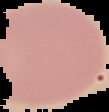
Summary:
  - Image type: segmented cell region with the area outside set to black
  - Result: no malaria parasites seen
  - Image size: 109×112 pixels
  - Preparation: thin blood film